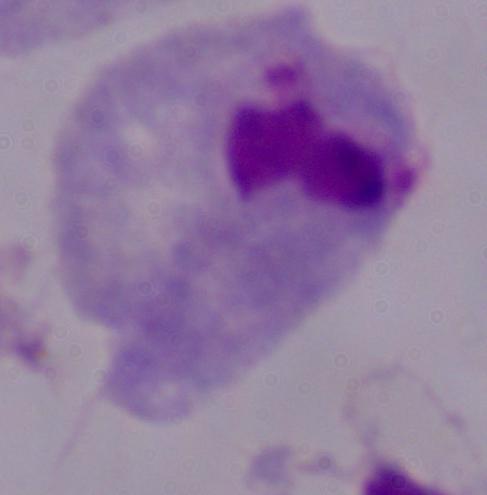
Captured at 1000x magnification. A trichomonad is seen. Photomicrograph.